Classify this cell by malaria status.
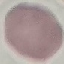
It is uninfected.

stain: Giemsa
capture: smartphone camera at the microscope eyepiece
preparation: thin blood smear
image_type: cell patch, automatically extracted from a larger field of view and resized to 64 × 64 pixels